Report the malaria status of this cell.
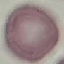

Uninfected.

Summary:
  - Preparation: thin blood film
  - Stain: Giemsa
  - Image type: automatically extracted cell patch, resized to 64 × 64 pixels
  - Capture: smartphone camera at the microscope eyepiece